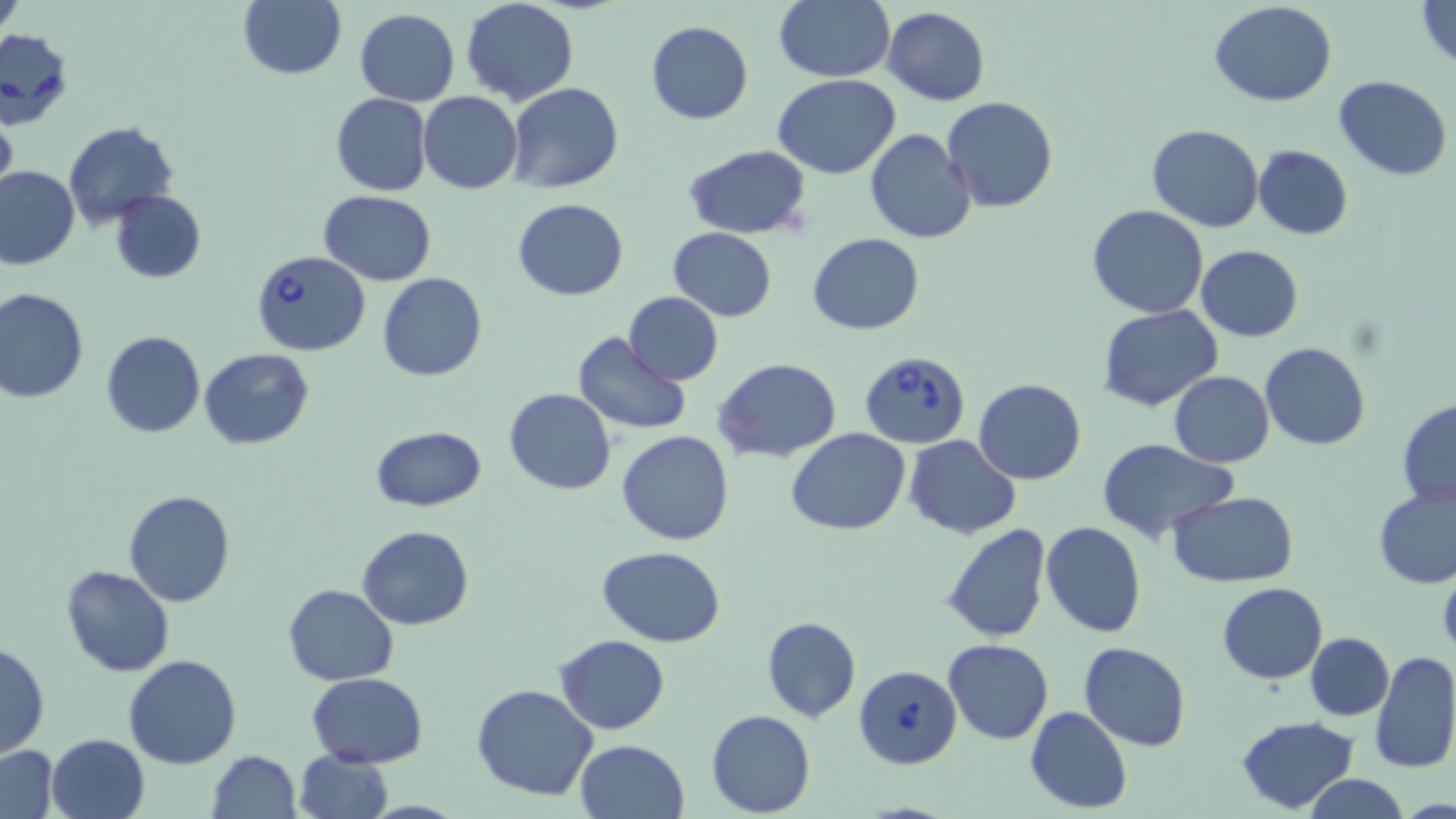
Summary:
  - Coordinate format: approximate bounding boxes as (x1, y1, x2, y2) in pixels
  - Uninfected red blood cell locations: (239, 0, 346, 80), (460, 0, 579, 106), (772, 0, 894, 82), (1412, 0, 1456, 71), (1209, 1, 1338, 106), (882, 7, 990, 106), (353, 8, 459, 106), (645, 20, 754, 124), (773, 74, 900, 178), (1333, 74, 1453, 179), (507, 82, 623, 195), (418, 92, 523, 193), (330, 93, 432, 195), (941, 96, 1058, 212), (0, 110, 17, 202), (63, 122, 177, 229), (1147, 124, 1263, 232), (865, 129, 977, 244), (682, 144, 813, 239), (1253, 145, 1353, 239), (0, 166, 80, 269), (109, 189, 206, 284), (319, 191, 436, 285), (513, 198, 628, 300), (1086, 203, 1212, 318), (667, 228, 777, 321), (809, 232, 925, 334), (1195, 245, 1303, 341), (376, 272, 486, 383), (0, 287, 89, 404), (623, 293, 724, 382), (1097, 306, 1223, 412), (101, 330, 205, 439), (572, 331, 691, 434), (1260, 343, 1369, 450), (200, 348, 314, 450), (714, 358, 841, 462), (1169, 371, 1275, 468), (974, 379, 1086, 485), (503, 389, 616, 494), (1397, 400, 1456, 506), (372, 426, 486, 510), (786, 429, 911, 534), (616, 430, 736, 546), (902, 435, 1021, 538), (1095, 438, 1239, 544), (1374, 487, 1456, 590), (122, 490, 235, 608), (1167, 491, 1299, 586), (1042, 521, 1148, 637), (941, 523, 1052, 643), (357, 525, 474, 631), (598, 546, 726, 647), (61, 564, 175, 677), (1438, 565, 1456, 660), (1217, 581, 1327, 683), (283, 583, 399, 685), (760, 616, 862, 723), (1305, 632, 1394, 720), (555, 634, 670, 734), (943, 638, 1054, 743), (0, 640, 50, 759), (1080, 641, 1191, 751), (1370, 650, 1456, 774), (123, 655, 241, 770), (306, 672, 428, 768), (472, 684, 599, 802), (1025, 706, 1133, 814), (706, 710, 815, 817), (1233, 715, 1359, 813), (46, 733, 150, 819), (574, 739, 689, 819), (1, 744, 61, 818), (292, 750, 394, 819), (206, 751, 301, 819), (1302, 773, 1410, 819)
  - Babesia divergens-infected red blood cell locations: (1, 32, 72, 133), (246, 253, 370, 358), (861, 352, 972, 451), (853, 664, 962, 769)
  - Slide-level diagnosis: Babesia divergens
  - Magnification: 1000x
  - Field of view: single
  - Image size: 1456×819 pixels
  - Stain: May-Grünwald-Giemsa
  - Preparation: thin blood smear
  - Modality: optical microscopy